Classify this cell by malaria status.
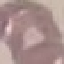
Uninfected.

Cell patch, automatically extracted from a larger field of view and resized to 64 × 64 pixels. Thin blood film. Giemsa stain. Acquired by smartphone through the microscope eyepiece.